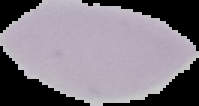
Summary:
  - Image size: 199×106 pixels
  - Result: no malaria parasites seen
  - Preparation: thin blood film
  - Image type: segmented cell region on a black background